Locate and identify every blood parasite.
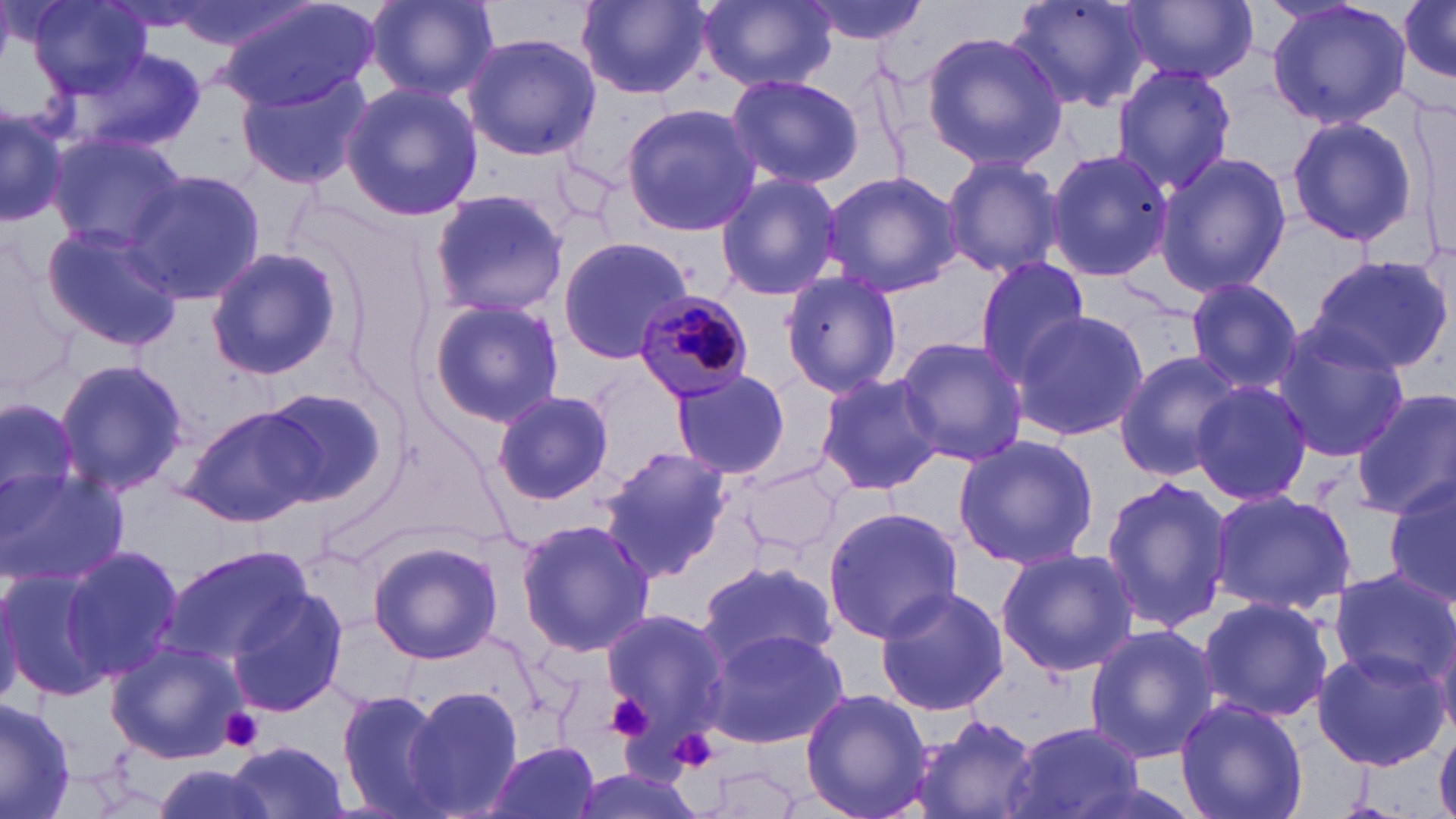
Approximate bounding boxes as (x1, y1, x2, y2) in pixels.
Plasmodium malariae-infected red blood cells: (630, 293, 757, 402).
No Plasmodium falciparum, Plasmodium ovale, Plasmodium vivax, Babesia divergens, or Trypanosoma brucei observed.

slide-level diagnosis = Plasmodium malariae
platelet locations = approximate bounding boxes as (x1, y1, x2, y2) in pixels: (605, 691, 655, 741), (220, 707, 264, 752), (667, 725, 720, 777)
uninfected red blood cell locations = approximate bounding boxes as (x1, y1, x2, y2) in pixels: (365, 0, 499, 101), (576, 0, 710, 99), (696, 0, 840, 93), (800, 0, 930, 43), (1009, 0, 1160, 112), (1266, 0, 1410, 129), (25, 1, 152, 101), (219, 1, 377, 112), (1400, 1, 1455, 85), (1123, 3, 1255, 84), (919, 31, 1068, 170), (463, 32, 600, 162), (72, 46, 206, 156), (1110, 63, 1237, 194), (236, 71, 371, 190), (725, 71, 864, 190), (339, 82, 483, 219), (0, 100, 67, 227), (621, 103, 761, 237), (1285, 113, 1420, 249), (45, 130, 186, 251), (1045, 147, 1173, 283), (1156, 152, 1293, 297), (940, 153, 1065, 280), (124, 168, 265, 307), (820, 170, 962, 296), (714, 171, 844, 302), (428, 186, 573, 321), (42, 223, 186, 351), (557, 236, 696, 362), (204, 246, 340, 380), (0, 247, 80, 401), (1307, 252, 1454, 375), (973, 255, 1092, 380), (780, 270, 904, 397), (1185, 277, 1303, 392), (424, 296, 565, 428), (1010, 308, 1148, 441), (1271, 327, 1409, 460), (894, 336, 1030, 466), (1113, 352, 1242, 484), (53, 358, 189, 500), (669, 368, 793, 482), (813, 371, 943, 495), (1189, 380, 1315, 505), (256, 387, 390, 505), (491, 390, 613, 505), (1351, 390, 1456, 519), (1, 391, 88, 532), (181, 403, 328, 528), (952, 433, 1098, 571), (597, 448, 735, 579), (738, 460, 847, 559), (1, 467, 129, 586), (1384, 475, 1456, 611), (1099, 477, 1234, 633), (1210, 491, 1356, 613), (822, 505, 963, 646), (516, 519, 658, 656), (369, 538, 504, 665), (58, 543, 184, 684), (159, 543, 316, 672), (995, 548, 1137, 678), (697, 557, 840, 672), (0, 568, 116, 703), (1327, 568, 1455, 692), (873, 584, 1012, 717), (227, 589, 349, 717), (1195, 595, 1333, 723), (598, 609, 728, 735), (1083, 625, 1219, 763), (701, 628, 845, 750), (104, 639, 244, 764), (1311, 647, 1448, 771), (400, 684, 523, 819), (332, 687, 452, 819), (799, 687, 932, 819), (0, 697, 77, 817), (1174, 698, 1309, 819), (912, 714, 1042, 819), (1004, 720, 1145, 819), (1435, 729, 1456, 819), (484, 740, 603, 819), (228, 741, 353, 818), (146, 763, 278, 819)
modality = light microscopy
field of view = single
stain = May-Grünwald-Giemsa
magnification = 1000x
preparation = thin blood film
image size = 1456×819 pixels